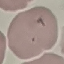
Summary:
  - Result: no malaria parasites detected
  - Preparation: thin blood smear
  - Capture: smartphone through the microscope eyepiece
  - Stain: Giemsa
  - Image type: automatically extracted cell patch, resized to 64 × 64 pixels